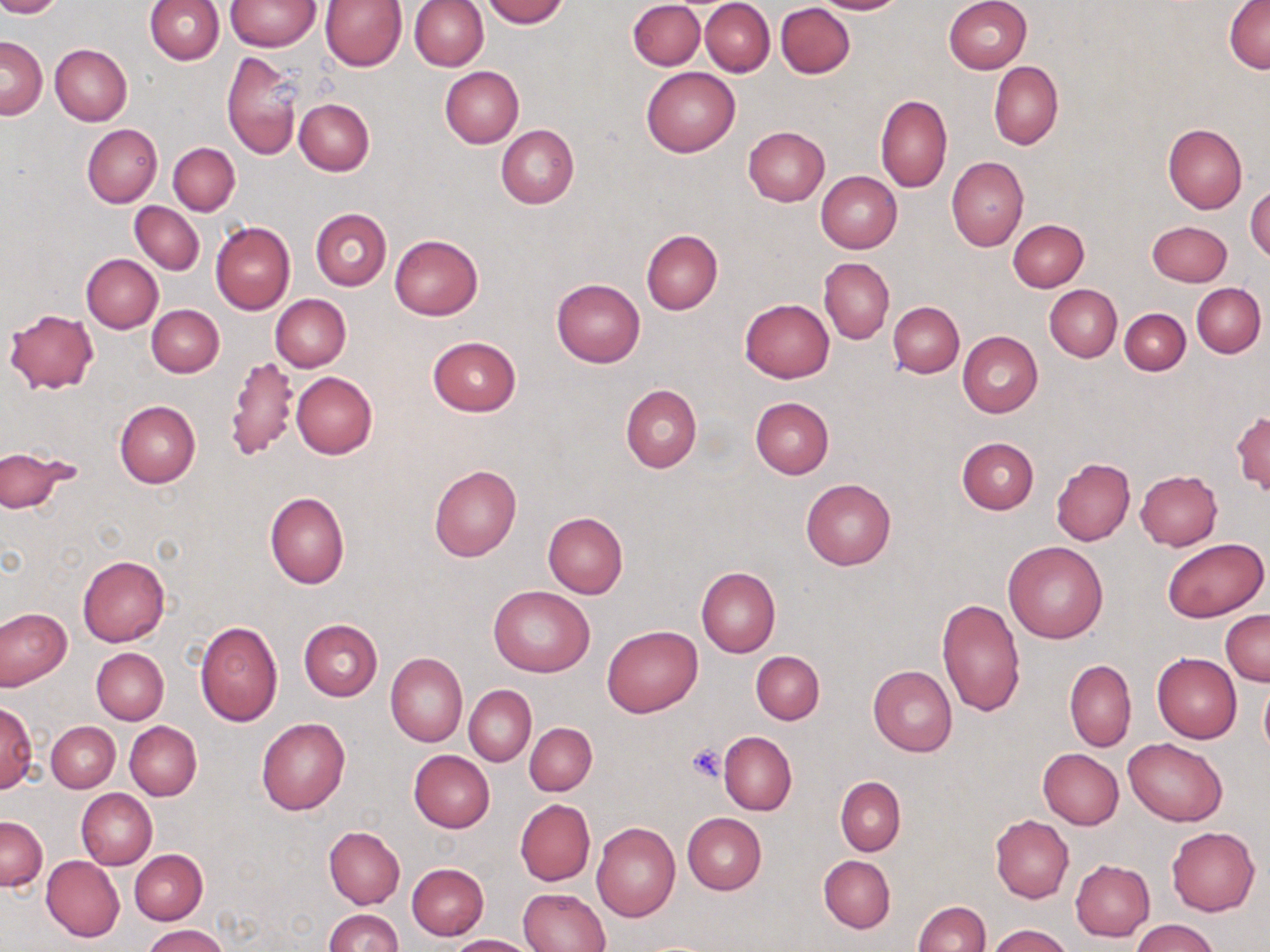 Approximate bounding boxes as [x1, y1, x2, y2] in pixels. Platelet locations: [686, 744, 727, 783]. Uninfected red blood cell locations: [0, 0, 62, 17], [145, 0, 225, 65], [482, 0, 568, 27], [701, 0, 775, 76], [814, 0, 906, 15], [1225, 0, 1269, 72], [226, 1, 320, 51], [318, 1, 406, 71], [409, 1, 488, 71], [628, 1, 704, 71], [945, 1, 1032, 73], [775, 2, 855, 79], [1, 35, 46, 119], [50, 44, 132, 125], [222, 51, 302, 161], [988, 61, 1063, 150], [439, 66, 524, 147], [641, 67, 740, 158], [876, 94, 952, 192], [295, 99, 374, 175], [83, 124, 162, 207], [496, 124, 578, 209], [1162, 124, 1247, 214], [743, 126, 830, 206], [168, 143, 239, 215], [946, 157, 1029, 250], [816, 172, 902, 253], [1246, 184, 1270, 262], [130, 201, 204, 274], [311, 209, 392, 291], [1009, 220, 1088, 292], [1148, 220, 1232, 285], [210, 221, 296, 314], [641, 229, 723, 314], [389, 234, 483, 320], [82, 253, 163, 333], [820, 257, 894, 343], [551, 278, 645, 366], [1192, 283, 1265, 358], [1044, 284, 1121, 361], [270, 294, 351, 372], [740, 298, 834, 382], [888, 301, 964, 377], [147, 305, 224, 377], [1120, 308, 1190, 374], [5, 309, 98, 393], [957, 331, 1043, 418], [427, 337, 521, 416], [224, 355, 299, 459], [291, 371, 377, 458], [621, 384, 702, 474], [749, 397, 834, 479], [115, 400, 202, 487], [1231, 411, 1269, 493], [956, 436, 1038, 514], [1, 447, 71, 512], [1050, 458, 1134, 546], [429, 464, 521, 561], [1135, 470, 1221, 551], [800, 479, 896, 571], [264, 491, 349, 590], [542, 511, 629, 597], [1161, 537, 1267, 622], [1003, 541, 1108, 642], [78, 555, 169, 645], [696, 566, 780, 658], [489, 585, 594, 677], [935, 597, 1025, 718], [0, 606, 72, 688], [1221, 610, 1269, 685], [297, 619, 383, 701], [194, 621, 284, 726], [602, 625, 702, 717], [92, 648, 168, 724], [752, 651, 824, 724], [385, 653, 467, 746], [1151, 653, 1241, 744], [1065, 659, 1136, 752], [868, 666, 958, 757], [1259, 674, 1270, 757], [464, 685, 536, 765], [1, 702, 35, 793], [256, 717, 350, 815], [46, 721, 120, 792], [125, 721, 202, 800], [524, 722, 597, 795], [718, 731, 796, 815], [1124, 738, 1226, 827], [1038, 749, 1124, 829], [408, 750, 494, 832], [835, 777, 905, 855], [76, 789, 156, 870], [515, 799, 595, 886], [682, 812, 767, 893], [1, 814, 47, 891], [990, 814, 1074, 902], [591, 821, 681, 921], [324, 827, 405, 908], [1166, 827, 1260, 916], [130, 849, 206, 924], [819, 855, 895, 933], [42, 856, 124, 941], [1071, 860, 1155, 942], [407, 863, 489, 939], [518, 887, 610, 952], [912, 901, 989, 952], [323, 909, 403, 952], [1131, 920, 1220, 952], [985, 924, 1073, 952], [142, 925, 230, 952], [446, 934, 534, 951]. Slide-level diagnosis: no evidence of blood parasites. Image is 1270×952 pixels. One field of a larger specimen. 1000x magnification. Optical microscopy. May-Grünwald-Giemsa-stained preparation. Thin blood film.